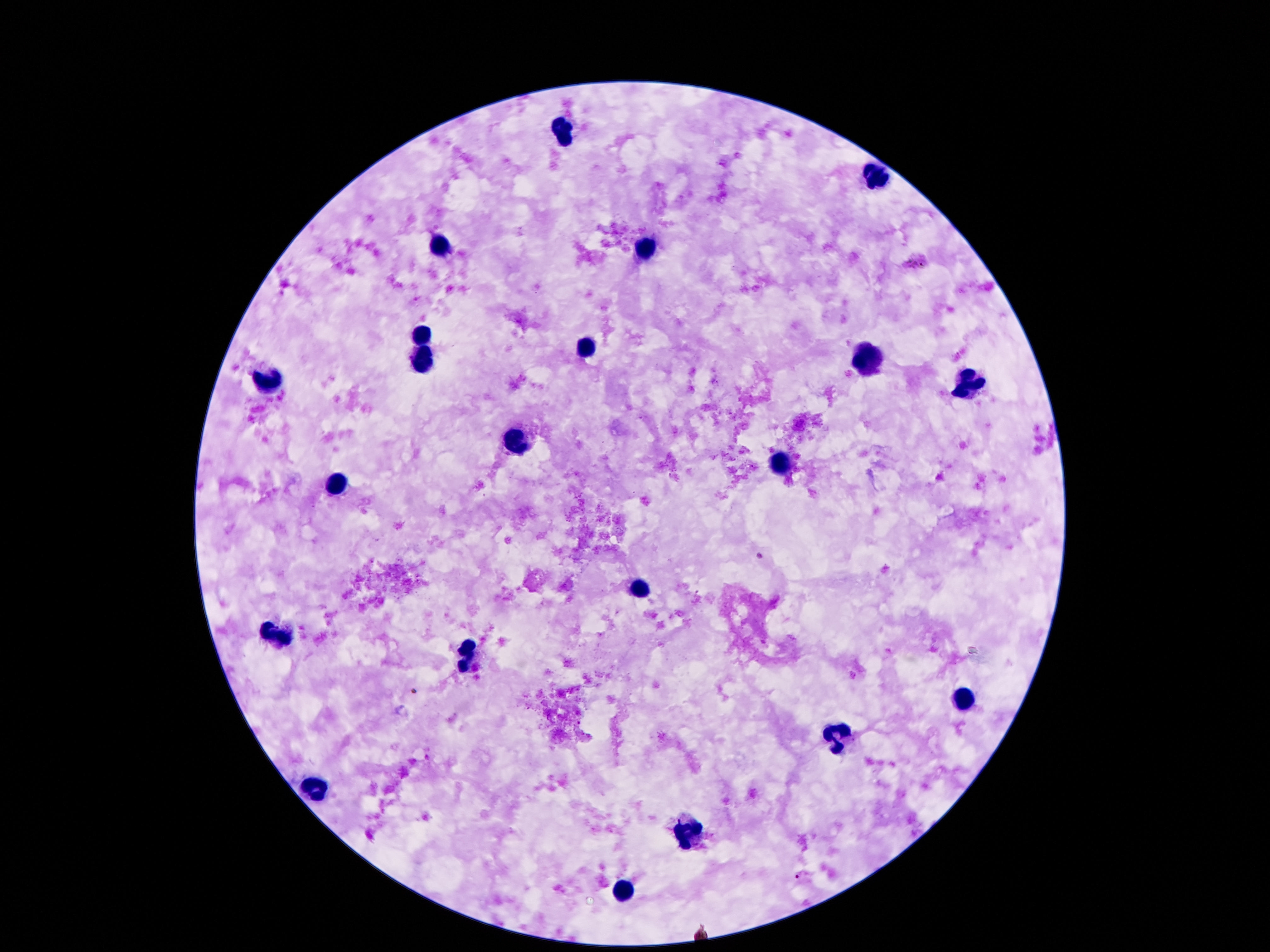

Approximate object centers, in pixels from the top-left corner.
Summary:
  - Leukocyte locations: (x=563, y=131), (x=873, y=176), (x=441, y=245), (x=645, y=253), (x=424, y=335), (x=586, y=345), (x=863, y=356), (x=422, y=364), (x=265, y=382), (x=968, y=384), (x=519, y=442), (x=779, y=461), (x=342, y=486), (x=638, y=587), (x=275, y=634), (x=466, y=655), (x=968, y=700), (x=840, y=737), (x=319, y=787), (x=686, y=835), (x=622, y=890)
  - Stain: Giemsa
  - Image size: 1270×952 pixels
  - Patient malaria status: uninfected
  - Field of view: single
  - Capture: smartphone camera through the microscope eyepiece
  - Magnification: 100x
  - Preparation: thick blood film